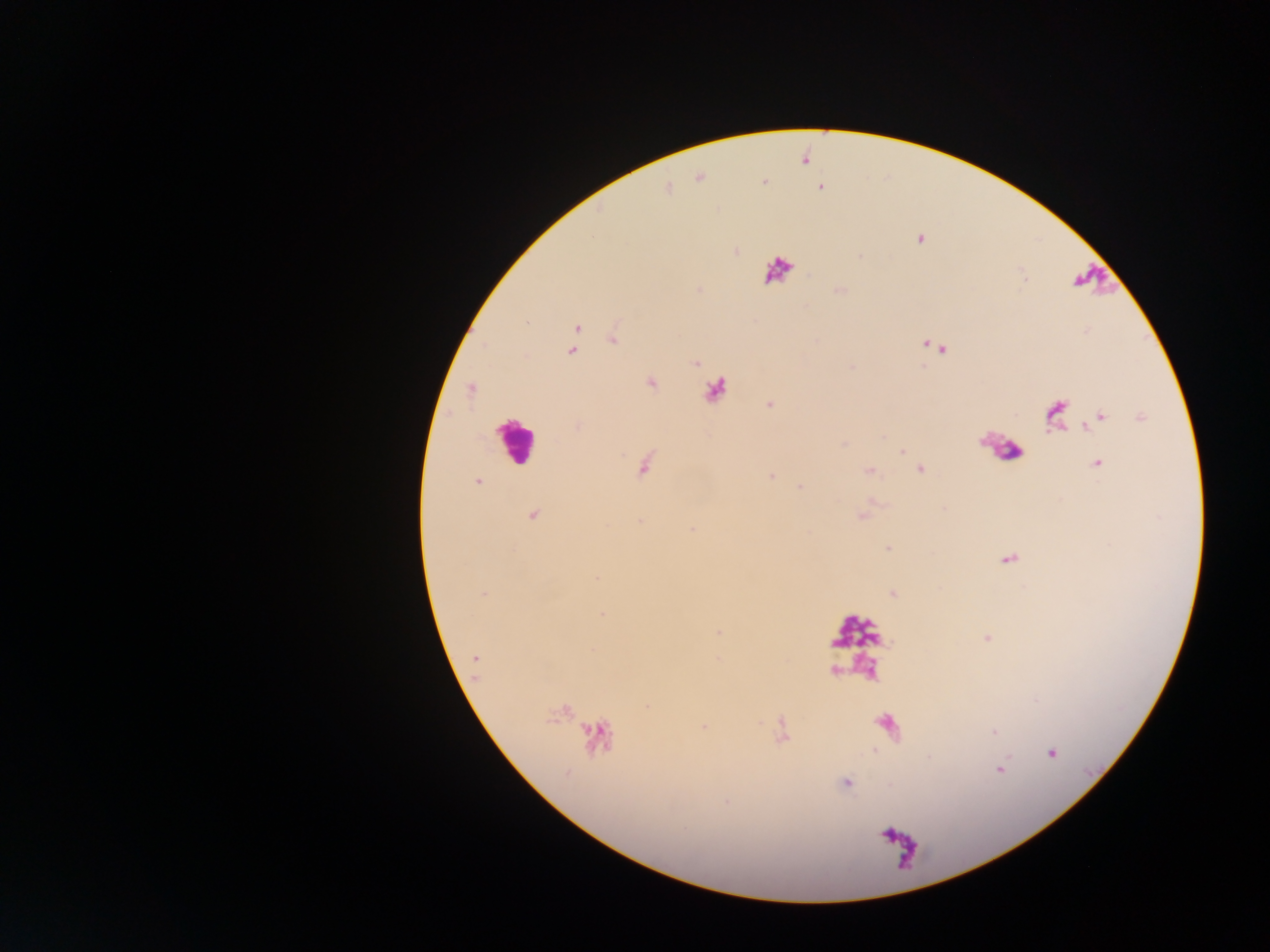
capture = mobile-phone photograph through a microscope
image size = 1270×952 pixels
leukocyte locations = approximate centers as (x, y) in pixels: (778, 269), (1095, 280), (515, 440), (999, 448), (856, 632), (889, 727), (900, 847)
preparation = thick blood smear
malaria parasite locations = approximate centers as (x, y) in pixels: (699, 178), (667, 188), (820, 188), (920, 239), (735, 251), (839, 290), (576, 327), (574, 335), (612, 338), (925, 345), (932, 346), (942, 349), (570, 351), (694, 362), (650, 382), (471, 388), (770, 404), (1054, 414), (1099, 416), (1139, 416), (578, 426), (902, 452), (1096, 464), (644, 465), (920, 469), (869, 471), (771, 475), (477, 481), (800, 487), (532, 513), (861, 515), (640, 519), (691, 528), (887, 548), (1008, 559), (892, 592), (484, 594), (601, 614), (718, 631), (986, 638), (475, 659), (702, 726), (994, 733), (1051, 753), (845, 783)
country = Ghana
field of view = single